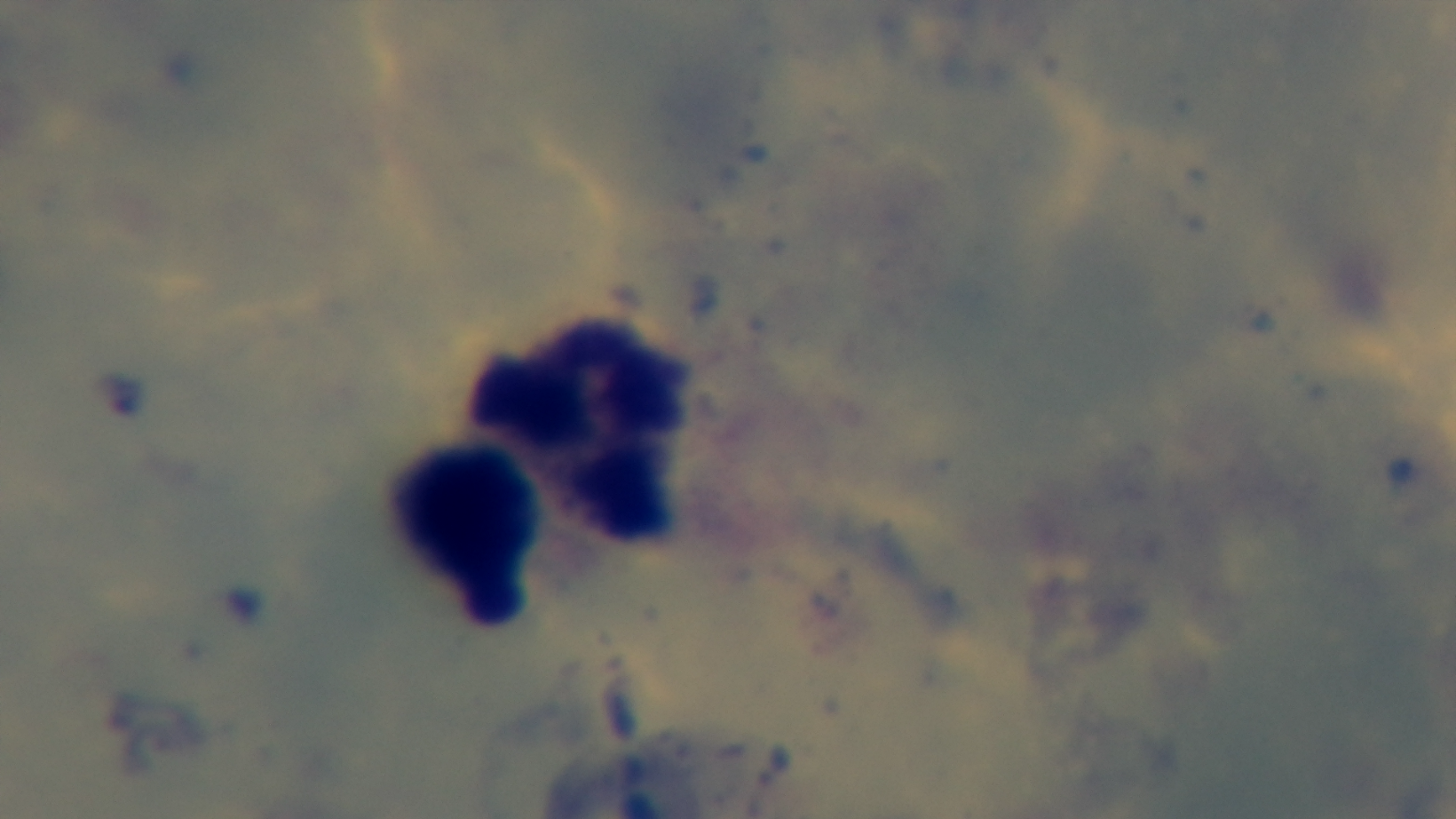
capture: mounted 4K digital camera
objective: 100x oil immersion
preparation: thick smear
modality: light microscopy
malaria_status: negative
stain: Giemsa
field_of_view: one from the slide